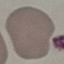
{
  "result": "no malaria parasites detected",
  "preparation": "thin blood film",
  "capture": "smartphone camera at the microscope eyepiece",
  "image_type": "cell patch, automatically extracted from a larger field of view and resized to 64 × 64 pixels",
  "stain": "Giemsa"
}